Locate and identify every blood parasite.
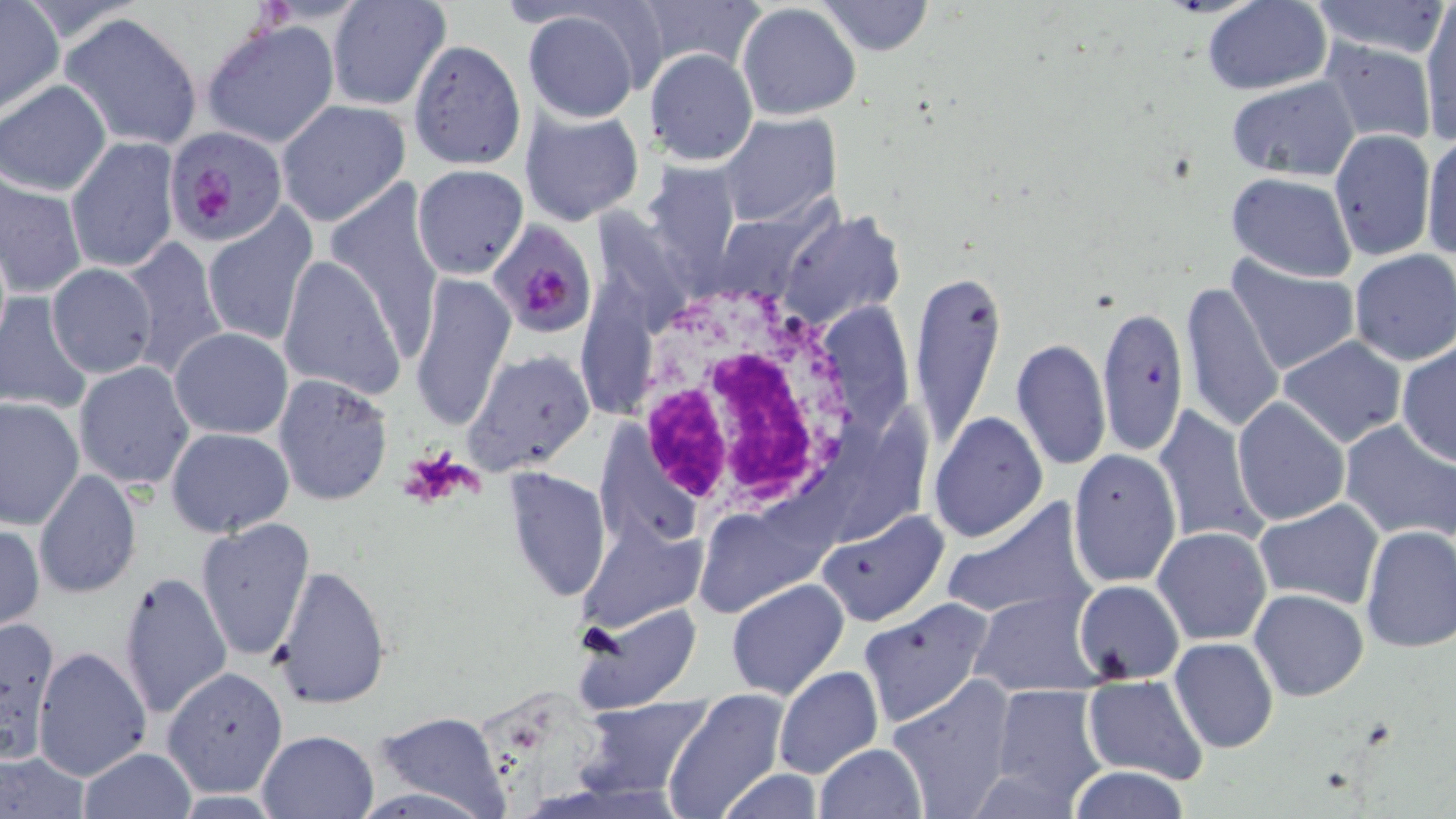
Approximate bounding boxes as (x1,y1)-(x2,y2) corner pairs in pixels.
Plasmodium falciparum-infected red blood cells: (165,125)-(289,247), (490,224)-(595,333).
No Plasmodium ovale, Plasmodium malariae, Plasmodium vivax, Babesia divergens, or Trypanosoma brucei observed.

Uninfected red blood cell locations: (636,0)-(762,78), (1201,0)-(1331,94), (326,1)-(451,111), (818,1)-(933,56), (1305,1)-(1451,59), (1418,2)-(1456,146), (1,3)-(63,112), (736,3)-(861,121), (522,10)-(643,122), (61,12)-(205,150), (202,18)-(341,149), (408,38)-(527,170), (1318,38)-(1439,143), (645,48)-(758,165), (1224,75)-(1361,183), (1,80)-(111,195), (276,101)-(409,226), (519,108)-(644,226), (716,113)-(841,226), (1329,130)-(1436,260), (1421,133)-(1456,264), (66,137)-(180,274), (642,161)-(748,285), (411,164)-(528,280), (1,172)-(86,299), (1225,172)-(1357,281), (325,185)-(442,368), (202,203)-(320,351), (779,211)-(906,334), (119,236)-(229,380), (1348,251)-(1456,365), (277,253)-(403,400), (1228,256)-(1361,377), (45,263)-(159,378), (908,268)-(1007,449), (409,273)-(514,434), (1180,280)-(1284,436), (0,295)-(93,413), (1095,303)-(1187,459), (169,328)-(292,439), (1277,337)-(1407,448), (1012,340)-(1111,470), (1397,341)-(1456,467), (465,350)-(596,474), (73,362)-(197,488), (272,374)-(394,506), (0,396)-(85,532), (1232,398)-(1350,527), (1152,404)-(1267,548), (930,410)-(1048,544), (1340,419)-(1456,543), (165,427)-(295,537), (1069,449)-(1182,589), (502,467)-(611,601), (33,469)-(142,599), (938,497)-(1098,626), (1254,499)-(1385,609), (693,507)-(821,615), (816,509)-(951,627), (195,517)-(316,663), (579,519)-(703,632), (0,523)-(45,632), (1360,525)-(1456,653), (1153,528)-(1271,645), (270,563)-(393,710), (118,571)-(231,721), (726,579)-(851,701), (1074,580)-(1186,684), (1249,588)-(1369,702), (970,594)-(1103,697), (858,598)-(996,728), (574,602)-(701,716), (0,614)-(62,764), (1169,637)-(1280,754), (33,646)-(151,781), (163,666)-(287,795), (774,666)-(884,781), (886,674)-(1019,818), (1085,675)-(1207,785), (988,684)-(1109,806), (661,689)-(786,819), (577,697)-(712,801), (372,711)-(510,819), (256,728)-(379,818), (813,743)-(927,819), (77,748)-(194,818), (0,753)-(89,817), (1067,766)-(1193,819), (713,768)-(827,819). White blood cell locations: (622,273)-(878,521). Platelet locations: (399,446)-(476,510). Slide-level diagnosis: Plasmodium falciparum. Image is 1456×819 pixels. May-Grünwald-Giemsa stain. Thin blood smear. One field of a larger specimen. Optical microscopy. Captured at 1000x magnification.